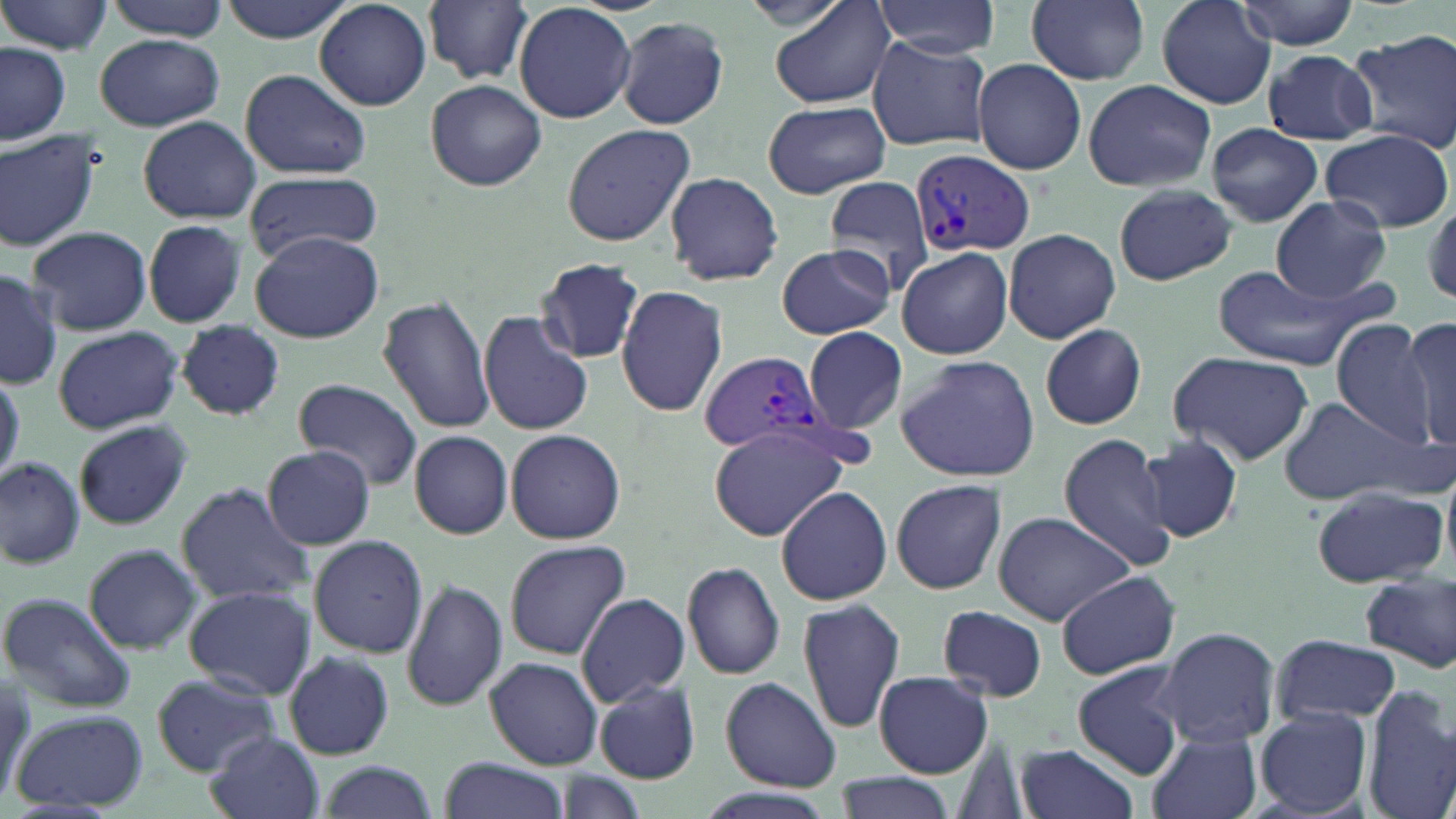 Approximate bounding boxes as [x1, y1, x2, y2] in pixels. Uninfected red blood cell locations: [102, 0, 231, 39], [216, 0, 354, 42], [768, 0, 896, 111], [875, 0, 1001, 56], [1024, 0, 1150, 85], [1153, 0, 1278, 108], [1235, 0, 1360, 50], [424, 1, 533, 85], [1, 2, 114, 57], [314, 2, 431, 109], [514, 2, 636, 124], [615, 15, 731, 129], [1349, 28, 1456, 152], [94, 35, 224, 131], [866, 35, 993, 152], [0, 43, 71, 143], [1261, 48, 1377, 143], [973, 61, 1087, 175], [239, 68, 371, 179], [1082, 77, 1216, 192], [425, 79, 547, 191], [763, 99, 891, 198], [138, 116, 260, 223], [1206, 122, 1323, 227], [560, 124, 695, 246], [1319, 128, 1454, 233], [0, 131, 104, 253], [244, 168, 382, 263], [662, 172, 784, 286], [823, 174, 938, 291], [1112, 184, 1237, 286], [1424, 193, 1456, 306], [1271, 197, 1392, 302], [142, 219, 249, 329], [27, 225, 151, 337], [1003, 227, 1121, 344], [249, 231, 381, 343], [776, 241, 894, 341], [896, 244, 1013, 360], [534, 257, 647, 364], [1210, 263, 1375, 369], [0, 267, 62, 387], [615, 283, 728, 418], [377, 294, 496, 435], [478, 311, 594, 436], [1333, 317, 1439, 444], [1400, 318, 1456, 448], [176, 321, 285, 420], [1039, 323, 1149, 429], [51, 326, 184, 435], [803, 327, 912, 433], [1166, 351, 1315, 465], [895, 353, 1041, 483], [0, 368, 24, 485], [294, 378, 424, 491], [1275, 394, 1435, 505], [74, 420, 191, 531], [708, 425, 853, 540], [507, 429, 625, 544], [409, 431, 513, 538], [1059, 433, 1176, 570], [1138, 434, 1244, 543], [261, 446, 376, 549], [0, 453, 87, 568], [891, 477, 1007, 595], [175, 482, 313, 606], [1310, 485, 1449, 588], [775, 486, 893, 604], [993, 509, 1134, 626], [309, 535, 428, 657], [503, 540, 632, 659], [81, 544, 205, 655], [682, 560, 786, 681], [1056, 571, 1180, 680], [1359, 573, 1456, 672], [402, 579, 507, 712], [183, 584, 316, 698], [0, 591, 137, 714], [577, 593, 690, 706], [799, 597, 907, 733], [937, 603, 1048, 702], [1154, 626, 1280, 749], [1272, 633, 1400, 727], [283, 649, 396, 759], [486, 657, 604, 769], [1071, 661, 1190, 779], [151, 671, 280, 774], [875, 671, 991, 777], [0, 672, 32, 810], [720, 678, 841, 791], [592, 679, 700, 784], [1361, 684, 1455, 819], [1255, 706, 1372, 818], [10, 710, 148, 812], [1144, 729, 1263, 819], [203, 730, 323, 819], [1015, 743, 1140, 819], [439, 756, 569, 819], [315, 760, 438, 819], [833, 772, 956, 819]. Plasmodium vivax-infected red blood cell locations: [911, 150, 1037, 259], [697, 350, 833, 456]. Slide-level diagnosis: Plasmodium vivax. One field of a larger specimen. Thin blood film. May-Grünwald-Giemsa stain. Optical microscopy. Captured at 1000x magnification. Image is 1456×819 pixels.